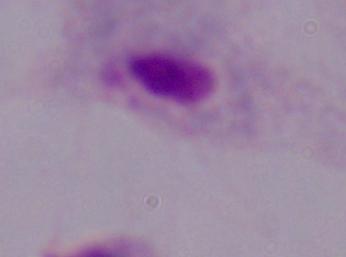

Summary:
  - Modality: photomicrograph
  - Magnification: 1000x
  - Identification: trichomonad